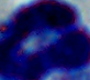 A leukocyte is shown. 1000x magnification. Photomicrograph.